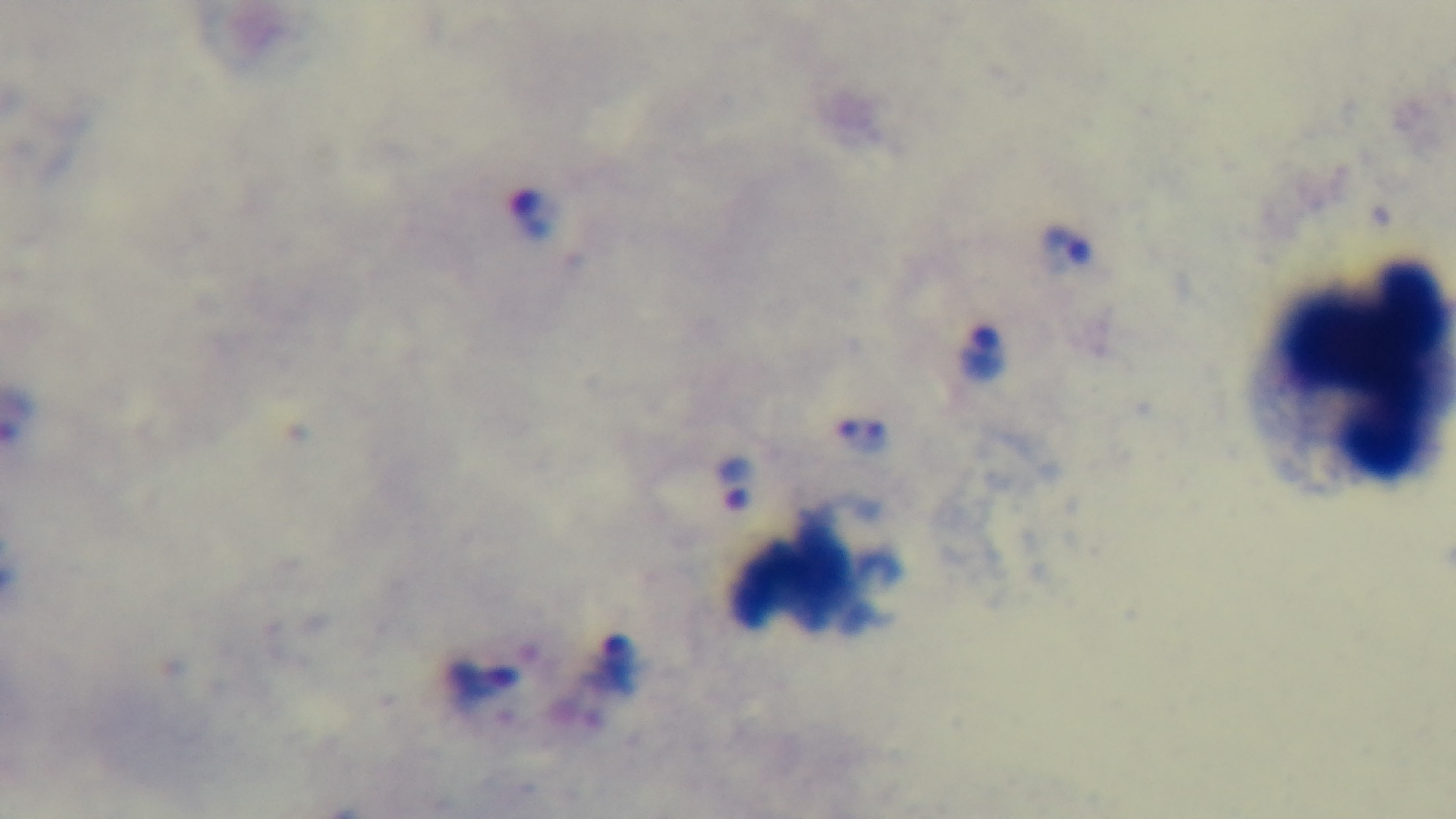 One field from the slide. 100x oil-immersion objective. Giemsa-stained. Mounted 4K digital camera. Light microscopy. Malaria status: positive. Preparation: thick smear.